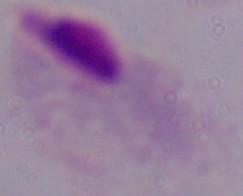 Photomicrograph. 1000x magnification. A trichomonad is seen.